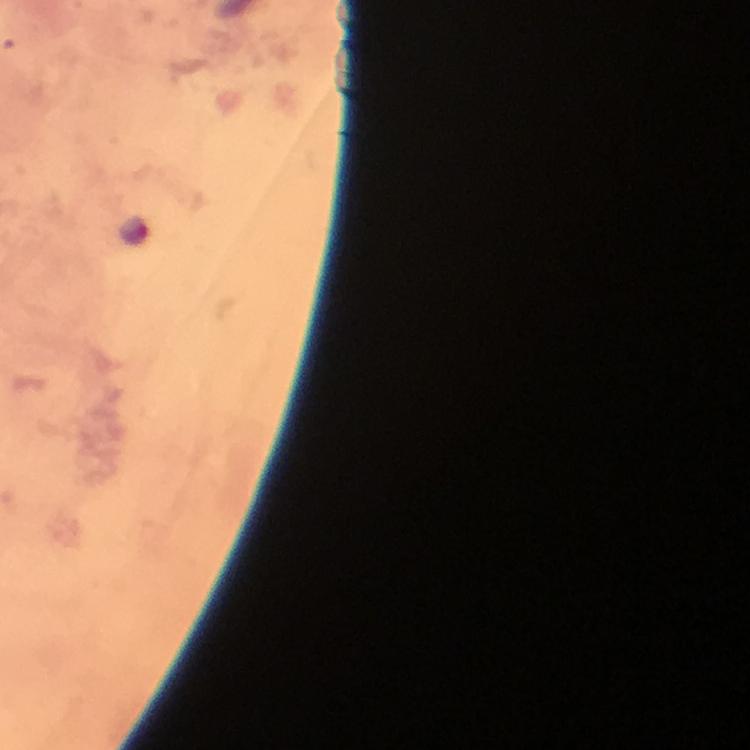
{
  "image_size": "750×750 pixels",
  "magnification": "100x",
  "capture": "smartphone camera through the microscope",
  "cropped_from": "a single field of view",
  "immersion_oil": "applied",
  "malaria_parasite_locations": "approximate centers as (x, y) in pixels: (134, 229)",
  "context": "from a malaria diagnostic workup",
  "stain": "Giemsa",
  "preparation": "thick blood film"
}